Assess the morphology of the erythrocytes.
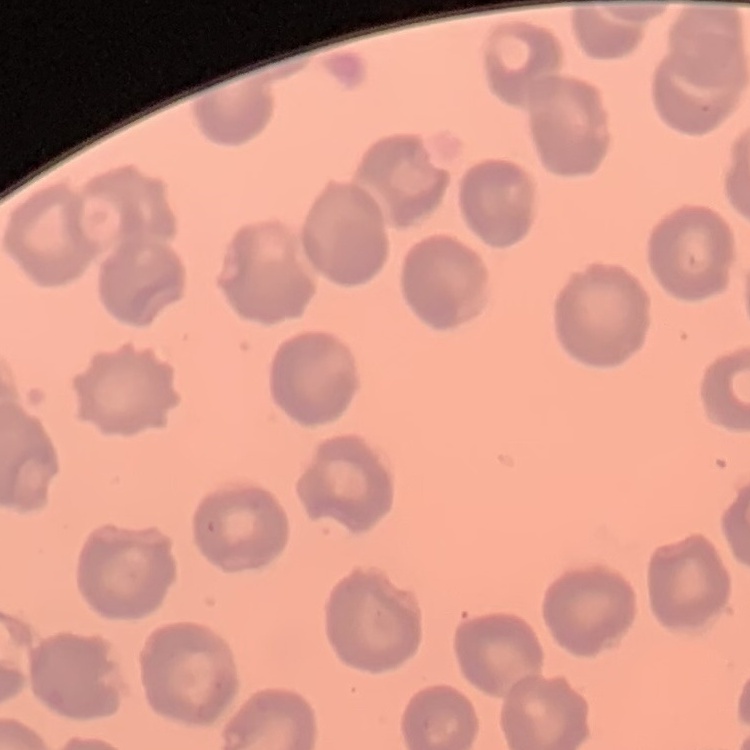

No rouleaux formation.

image type = square crop of a larger photomicrograph
preparation = thin blood smear
stain = Field's or Giemsa